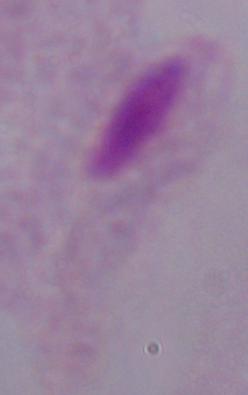

Micrograph. A trichomonad is seen. Captured at 1000x magnification.